Describe the morphology of the erythrocytes.
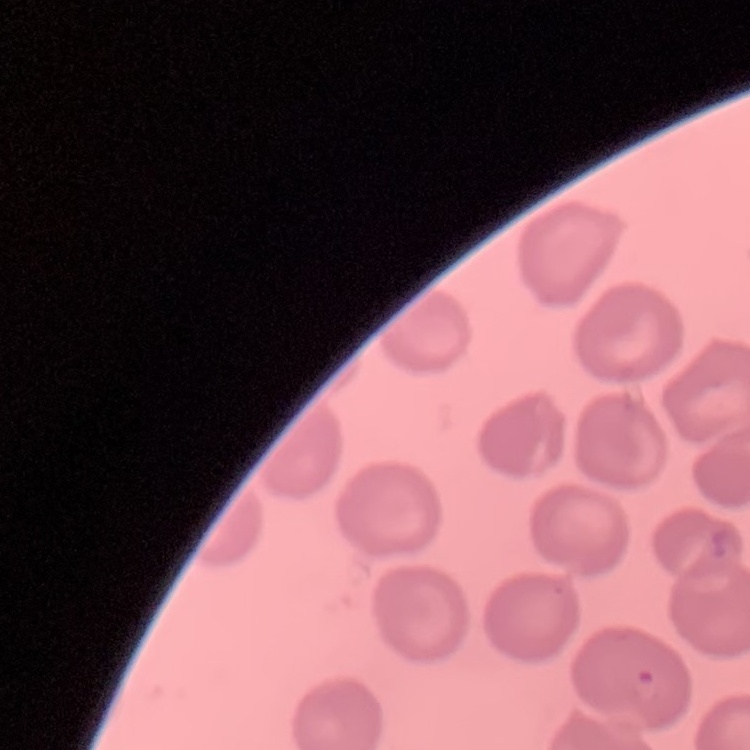

They show no rouleaux formation.

Field's or Giemsa stain. One tile cut from a larger photomicrograph. Thin peripheral smear.